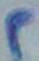 Photomicrograph. Captured at 1000x magnification. Toxoplasma gondii is shown.